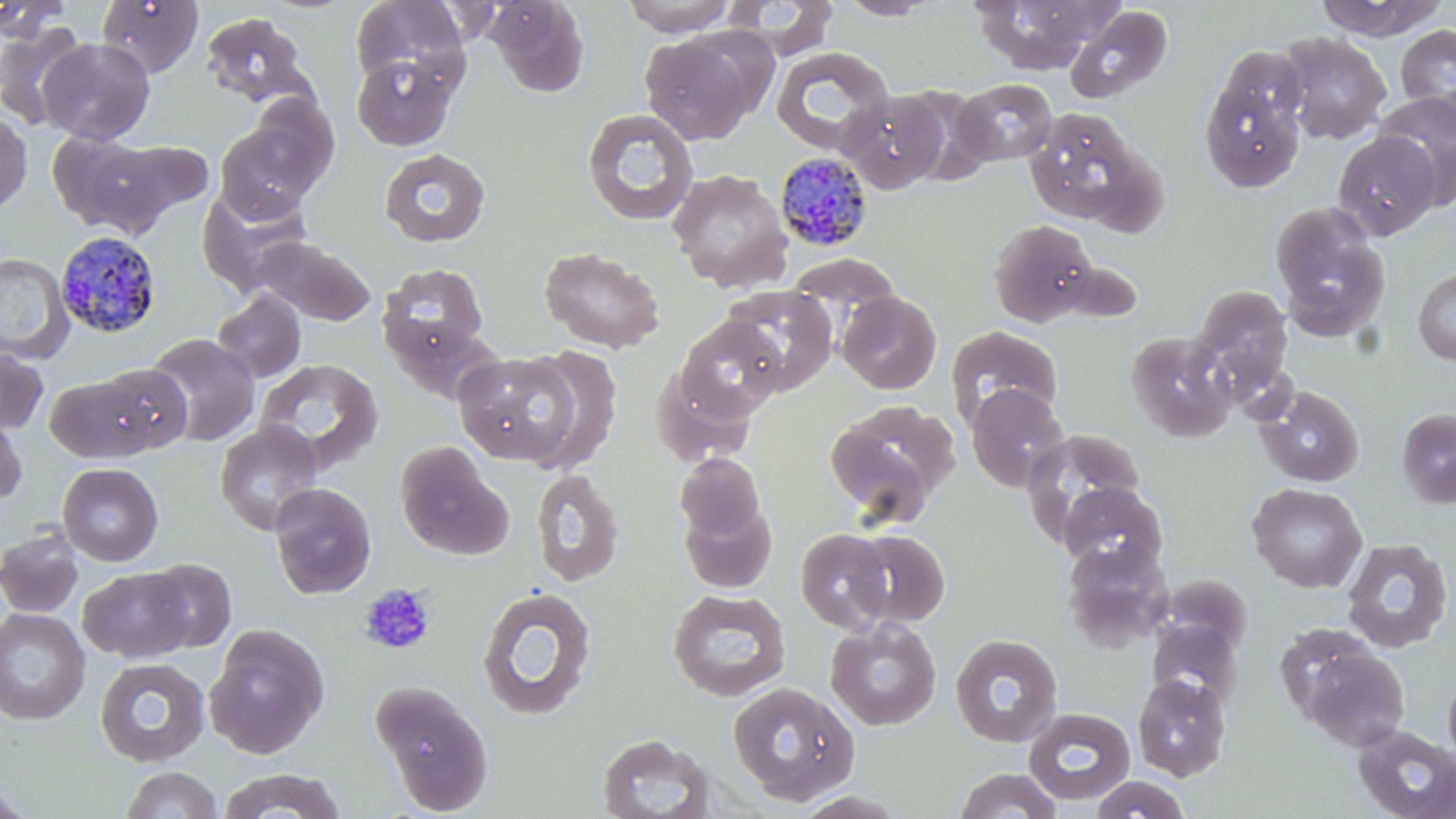 Approximate bounding boxes as (x1, y1, x2, y2) in pixels. Uninfected red blood cell locations: (95, 0, 204, 78), (350, 0, 469, 91), (484, 0, 590, 97), (619, 0, 738, 35), (720, 0, 839, 58), (835, 0, 942, 20), (968, 0, 1110, 75), (1312, 0, 1449, 41), (1065, 6, 1173, 104), (202, 12, 314, 107), (0, 19, 93, 130), (1395, 24, 1456, 124), (1277, 31, 1391, 143), (640, 32, 759, 145), (39, 38, 155, 144), (1218, 43, 1306, 131), (770, 46, 893, 156), (351, 54, 459, 151), (1199, 71, 1306, 194), (952, 78, 1057, 166), (895, 86, 997, 184), (838, 89, 948, 194), (1374, 91, 1456, 205), (240, 95, 340, 194), (1024, 107, 1144, 225), (582, 108, 699, 227), (0, 113, 32, 216), (214, 119, 324, 220), (45, 130, 167, 235), (1333, 131, 1439, 239), (93, 139, 213, 232), (378, 147, 492, 248), (667, 169, 793, 291), (196, 185, 314, 296), (1269, 202, 1390, 341), (988, 219, 1098, 327), (249, 235, 377, 327), (539, 246, 665, 353), (0, 253, 74, 363), (784, 253, 901, 317), (377, 263, 491, 371), (1413, 266, 1456, 366), (719, 284, 838, 396), (1191, 285, 1293, 389), (211, 289, 307, 384), (837, 291, 942, 394), (675, 316, 786, 422), (946, 324, 1064, 426), (1127, 331, 1237, 443), (143, 333, 260, 446), (520, 346, 624, 472), (0, 347, 49, 434), (453, 350, 583, 466), (253, 358, 383, 474), (91, 362, 193, 456), (652, 366, 758, 468), (44, 373, 161, 462), (966, 384, 1070, 492), (1255, 385, 1364, 487), (823, 400, 957, 523), (1395, 407, 1456, 509), (0, 410, 27, 509), (214, 421, 324, 535), (1020, 429, 1147, 543), (394, 441, 512, 561), (674, 453, 766, 544), (57, 463, 164, 566), (530, 468, 625, 588), (1059, 481, 1168, 573), (269, 482, 377, 599), (1247, 482, 1367, 593), (678, 498, 778, 594), (1, 527, 84, 618), (794, 528, 894, 633), (846, 528, 950, 627), (1341, 537, 1454, 652), (1061, 540, 1173, 651), (144, 558, 236, 652), (79, 566, 196, 663), (1157, 574, 1253, 655), (476, 586, 597, 721), (667, 588, 792, 701), (0, 607, 90, 724), (825, 618, 941, 731), (1146, 620, 1243, 711), (205, 626, 328, 758), (950, 633, 1063, 747), (1294, 639, 1411, 751), (94, 657, 210, 767), (1442, 667, 1456, 770), (1132, 674, 1231, 780), (371, 679, 495, 814), (728, 680, 860, 806), (1023, 708, 1135, 804), (1352, 725, 1456, 819), (595, 732, 717, 819), (120, 766, 223, 819), (217, 768, 347, 819), (952, 768, 1063, 818), (1089, 775, 1192, 818), (0, 779, 36, 819). Plasmodium malariae-infected red blood cell locations: (775, 151, 875, 253), (59, 229, 165, 338). Platelet locations: (358, 583, 436, 655). Slide-level diagnosis: Plasmodium malariae. Single field of view. May-Grünwald-Giemsa-stained preparation. Thin blood film. Image is 1456×819 pixels. Optical microscopy. Captured at 1000x magnification.